Report the malaria status.
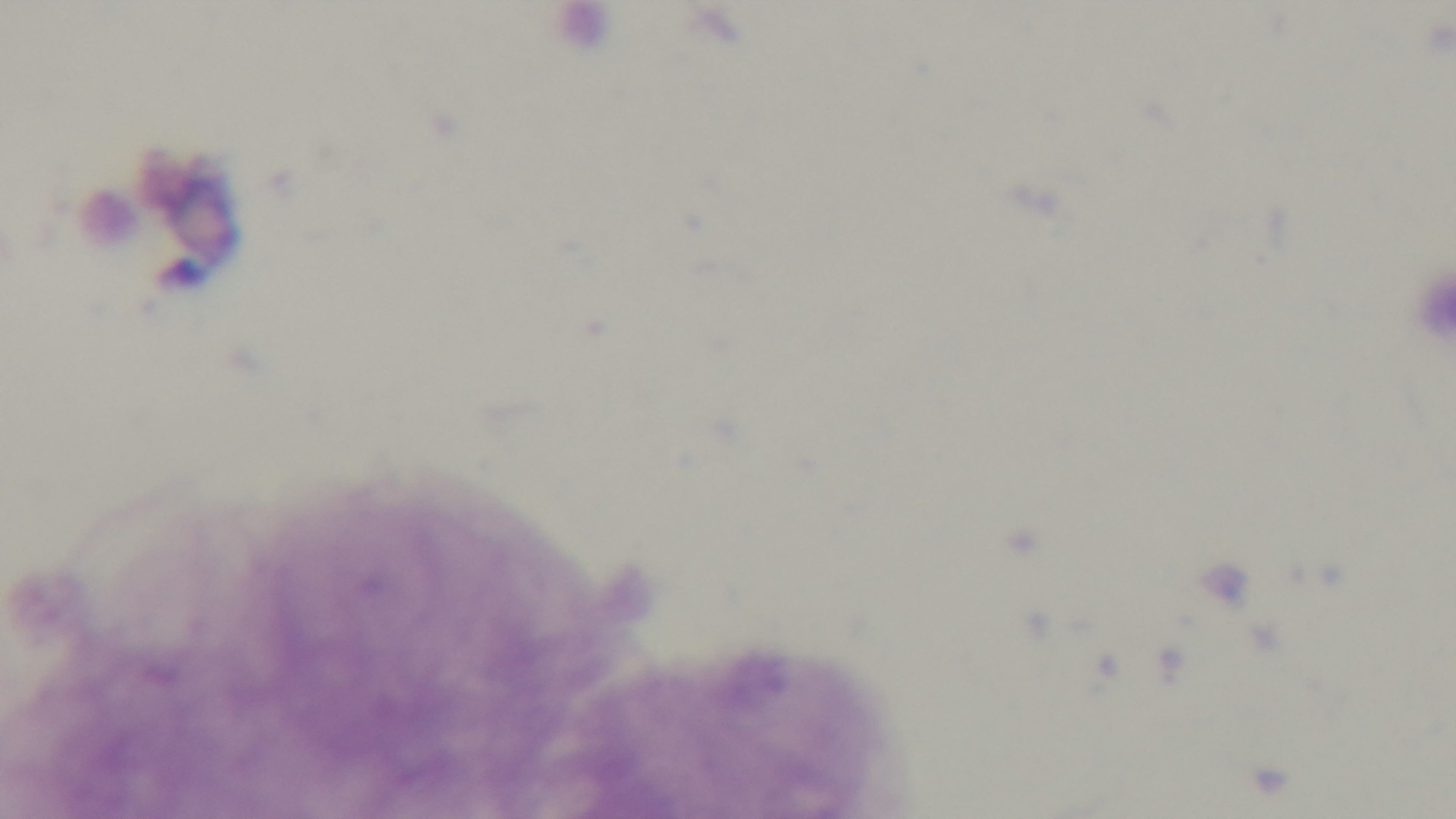

Negative.

preparation = thick smear
objective = 100x oil immersion
stain = Giemsa
modality = light microscopy
field of view = single
capture = mounted 4K digital camera